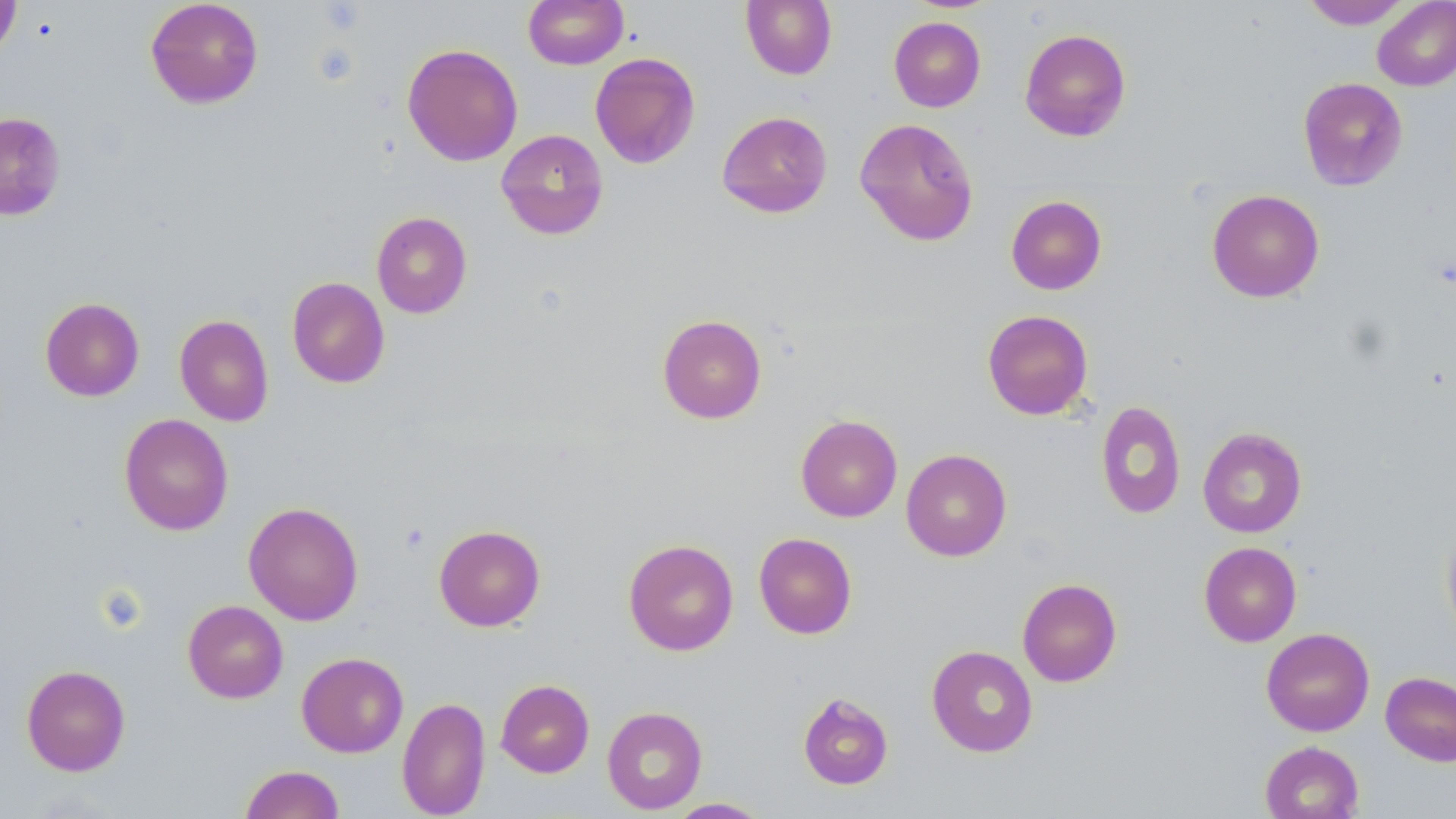
Summary:
  - Coordinate format: approximate bounding boxes as named x1/y1/x2/y2 corners in pixels
  - Uninfected red blood cell locations: (x1=0, y1=0, x2=20, y2=60), (x1=145, y1=0, x2=264, y2=108), (x1=523, y1=0, x2=629, y2=69), (x1=740, y1=0, x2=837, y2=80), (x1=1300, y1=0, x2=1413, y2=29), (x1=1372, y1=0, x2=1456, y2=91), (x1=889, y1=16, x2=986, y2=112), (x1=1019, y1=28, x2=1132, y2=142), (x1=402, y1=43, x2=523, y2=166), (x1=590, y1=52, x2=701, y2=169), (x1=1297, y1=77, x2=1408, y2=191), (x1=717, y1=111, x2=833, y2=218), (x1=0, y1=112, x2=66, y2=220), (x1=854, y1=118, x2=979, y2=246), (x1=496, y1=129, x2=609, y2=240), (x1=1206, y1=189, x2=1325, y2=302), (x1=1006, y1=195, x2=1107, y2=295), (x1=371, y1=211, x2=472, y2=318), (x1=287, y1=277, x2=390, y2=388), (x1=40, y1=297, x2=144, y2=401), (x1=982, y1=310, x2=1094, y2=420), (x1=174, y1=314, x2=274, y2=426), (x1=657, y1=314, x2=767, y2=424), (x1=1096, y1=400, x2=1186, y2=520), (x1=119, y1=413, x2=234, y2=535), (x1=795, y1=414, x2=902, y2=522), (x1=1198, y1=427, x2=1307, y2=538), (x1=901, y1=449, x2=1012, y2=561), (x1=243, y1=502, x2=364, y2=625), (x1=1441, y1=521, x2=1456, y2=644), (x1=434, y1=525, x2=545, y2=631), (x1=753, y1=532, x2=857, y2=639), (x1=623, y1=538, x2=739, y2=656), (x1=1199, y1=542, x2=1302, y2=646), (x1=1017, y1=578, x2=1122, y2=687), (x1=182, y1=600, x2=288, y2=703), (x1=1261, y1=628, x2=1374, y2=736), (x1=926, y1=645, x2=1038, y2=757), (x1=297, y1=652, x2=408, y2=757), (x1=21, y1=664, x2=131, y2=776), (x1=1381, y1=671, x2=1456, y2=767), (x1=495, y1=679, x2=594, y2=777), (x1=798, y1=692, x2=894, y2=790), (x1=397, y1=696, x2=490, y2=818), (x1=602, y1=706, x2=707, y2=814), (x1=1259, y1=741, x2=1364, y2=819), (x1=240, y1=765, x2=344, y2=818), (x1=667, y1=798, x2=771, y2=818)
  - Platelet locations: (x1=399, y1=522, x2=430, y2=554)
  - Slide-level diagnosis: no evidence of blood parasites
  - Field of view: single
  - Image size: 1456×819 pixels
  - Preparation: thin blood film
  - Magnification: 1000x
  - Stain: May-Grünwald-Giemsa
  - Modality: light microscopy